State the blood parasite species.
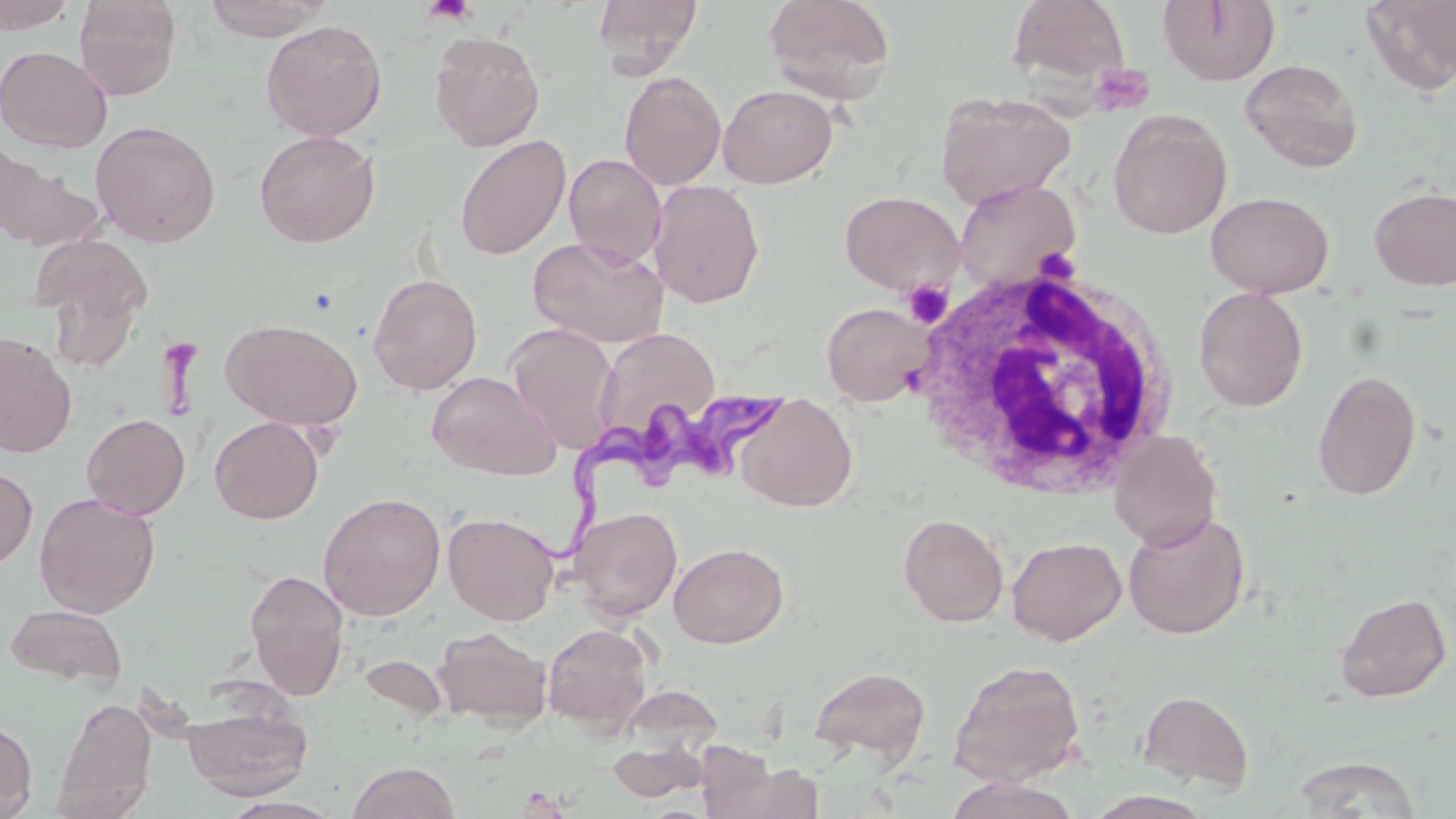
Trypanosoma brucei.

magnification = 1000x
Trypanosoma brucei locations = approximate bounding boxes as named x1/y1/x2/y2 corners in pixels: (x1=512, y1=384, x2=795, y2=572)
field of view = one of a larger specimen
stain = May-Grünwald-Giemsa
preparation = thin blood film
uninfected red blood cell locations = approximate bounding boxes as named x1/y1/x2/y2 corners in pixels: (x1=0, y1=0, x2=78, y2=34), (x1=73, y1=0, x2=182, y2=100), (x1=201, y1=0, x2=336, y2=41), (x1=593, y1=0, x2=703, y2=76), (x1=763, y1=0, x2=898, y2=102), (x1=1359, y1=0, x2=1456, y2=97), (x1=1006, y1=1, x2=1131, y2=88), (x1=1157, y1=1, x2=1281, y2=87), (x1=260, y1=19, x2=387, y2=141), (x1=428, y1=30, x2=546, y2=151), (x1=0, y1=45, x2=112, y2=152), (x1=1239, y1=59, x2=1363, y2=172), (x1=619, y1=72, x2=727, y2=190), (x1=717, y1=84, x2=839, y2=189), (x1=934, y1=91, x2=1076, y2=208), (x1=1108, y1=109, x2=1232, y2=239), (x1=90, y1=119, x2=221, y2=247), (x1=254, y1=130, x2=380, y2=248), (x1=454, y1=134, x2=572, y2=260), (x1=0, y1=145, x2=101, y2=251), (x1=564, y1=154, x2=666, y2=267), (x1=951, y1=178, x2=1081, y2=293), (x1=649, y1=179, x2=765, y2=308), (x1=1368, y1=185, x2=1456, y2=290), (x1=840, y1=190, x2=963, y2=295), (x1=1205, y1=191, x2=1334, y2=297), (x1=27, y1=232, x2=153, y2=351), (x1=528, y1=236, x2=668, y2=347), (x1=368, y1=273, x2=482, y2=395), (x1=1193, y1=287, x2=1309, y2=412), (x1=821, y1=302, x2=934, y2=406), (x1=223, y1=318, x2=362, y2=431), (x1=506, y1=323, x2=619, y2=453), (x1=594, y1=327, x2=720, y2=444), (x1=0, y1=331, x2=77, y2=459), (x1=1312, y1=369, x2=1421, y2=501), (x1=427, y1=371, x2=560, y2=480), (x1=735, y1=396, x2=857, y2=511), (x1=81, y1=413, x2=190, y2=519), (x1=210, y1=416, x2=324, y2=524), (x1=1109, y1=430, x2=1222, y2=550), (x1=0, y1=465, x2=38, y2=570), (x1=34, y1=492, x2=161, y2=617), (x1=318, y1=492, x2=446, y2=620), (x1=569, y1=506, x2=682, y2=622), (x1=1122, y1=510, x2=1252, y2=639), (x1=443, y1=511, x2=560, y2=625), (x1=898, y1=513, x2=1008, y2=627), (x1=1006, y1=536, x2=1127, y2=645), (x1=669, y1=542, x2=789, y2=648), (x1=244, y1=568, x2=350, y2=699), (x1=1334, y1=592, x2=1452, y2=703), (x1=4, y1=603, x2=128, y2=689), (x1=543, y1=623, x2=654, y2=736), (x1=432, y1=626, x2=552, y2=730), (x1=358, y1=654, x2=451, y2=721), (x1=948, y1=659, x2=1086, y2=785), (x1=808, y1=665, x2=931, y2=766), (x1=616, y1=683, x2=724, y2=763), (x1=1136, y1=689, x2=1255, y2=793), (x1=180, y1=695, x2=313, y2=800), (x1=52, y1=697, x2=158, y2=817), (x1=0, y1=719, x2=37, y2=818), (x1=606, y1=739, x2=710, y2=802), (x1=1291, y1=755, x2=1422, y2=817), (x1=710, y1=757, x2=825, y2=818), (x1=348, y1=761, x2=461, y2=819), (x1=943, y1=776, x2=1082, y2=819), (x1=220, y1=795, x2=344, y2=819)
modality = optical microscopy
platelet locations = approximate bounding boxes as named x1/y1/x2/y2 corners in pixels: (x1=421, y1=0, x2=476, y2=25), (x1=1088, y1=63, x2=1156, y2=117), (x1=901, y1=278, x2=954, y2=328), (x1=516, y1=786, x2=571, y2=818)
image size = 1456×819 pixels
white blood cell locations = approximate bounding boxes as named x1/y1/x2/y2 corners in pixels: (x1=909, y1=262, x2=1181, y2=501)